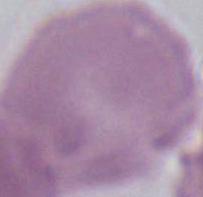 Micrograph. Captured at 1000x magnification. A red blood cell is shown.